Assess this cell for malaria.
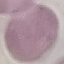

It is uninfected.

preparation = thin smear
capture = smartphone camera at the microscope eyepiece
stain = Giemsa
image type = automatically extracted cell patch, resized to 64 × 64 pixels